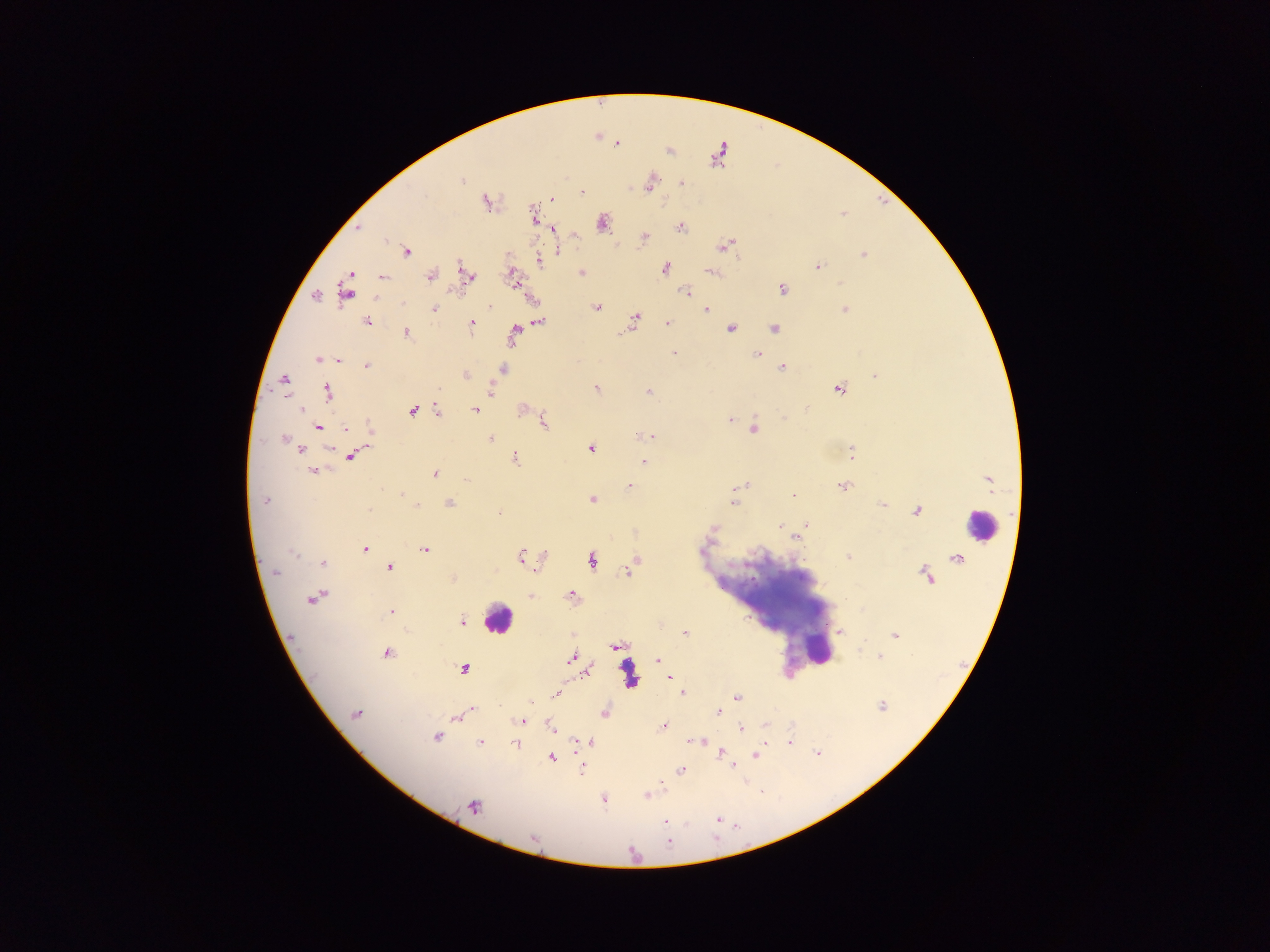
{
  "capture": "mobile-phone photograph through a microscope",
  "country": "Ghana",
  "image_size": "1270×952 pixels",
  "leukocyte_locations": "approximate centers as [x, y] in pixels: [980, 525], [497, 619], [815, 651]",
  "field_of_view": "single",
  "malaria_parasite_locations": "approximate centers as [x, y] in pixels: [617, 143], [461, 181], [682, 182], [650, 184], [581, 191], [551, 198], [486, 201], [533, 214], [602, 224], [680, 228], [553, 229], [645, 237], [387, 240], [725, 245], [407, 252], [559, 252], [864, 255], [539, 262], [818, 266], [665, 268], [710, 271], [581, 272], [467, 275], [430, 276], [382, 277], [516, 283], [781, 289], [346, 291], [685, 292], [315, 295], [403, 303], [489, 307], [597, 308], [433, 309], [706, 309], [844, 310], [635, 318], [368, 321], [539, 322], [668, 323], [472, 324], [730, 328], [774, 328], [514, 332], [407, 333], [674, 353], [757, 354], [319, 360], [338, 360], [366, 366], [782, 367], [503, 370], [465, 375], [875, 375], [284, 379], [439, 389], [596, 389], [839, 389], [490, 391], [649, 391], [327, 392], [301, 410], [475, 410], [438, 411], [412, 412], [782, 417], [730, 420], [543, 421], [318, 427], [370, 428], [346, 429], [754, 430], [644, 435], [651, 436], [490, 438], [284, 439], [591, 449], [301, 450], [852, 453], [351, 456], [515, 458], [643, 462], [313, 470], [434, 474], [746, 484], [629, 485], [843, 486], [401, 493], [793, 494], [591, 500], [265, 501], [734, 502], [449, 503], [883, 505], [417, 506], [369, 509], [917, 511], [498, 513], [807, 524], [780, 525], [712, 528], [797, 537], [365, 549], [425, 549], [293, 555], [521, 556], [848, 556], [591, 560], [323, 563], [389, 568], [628, 571], [275, 572], [571, 595], [530, 596], [315, 597], [391, 612], [462, 622], [838, 630], [684, 633], [894, 635], [615, 645], [387, 654], [880, 656], [571, 658], [658, 659], [463, 669], [586, 671], [669, 677], [682, 692], [557, 695], [736, 698], [531, 703], [883, 706], [473, 709], [718, 712], [604, 713], [355, 714], [457, 718], [521, 720], [663, 727], [552, 729], [741, 729], [436, 737], [699, 741], [590, 742], [692, 742], [790, 742], [480, 743], [517, 745], [721, 752], [818, 753], [755, 754], [552, 758], [732, 766], [680, 770], [582, 771], [662, 786], [646, 795], [603, 799], [474, 806], [717, 819], [665, 822], [668, 843]",
  "preparation": "thick blood film"
}